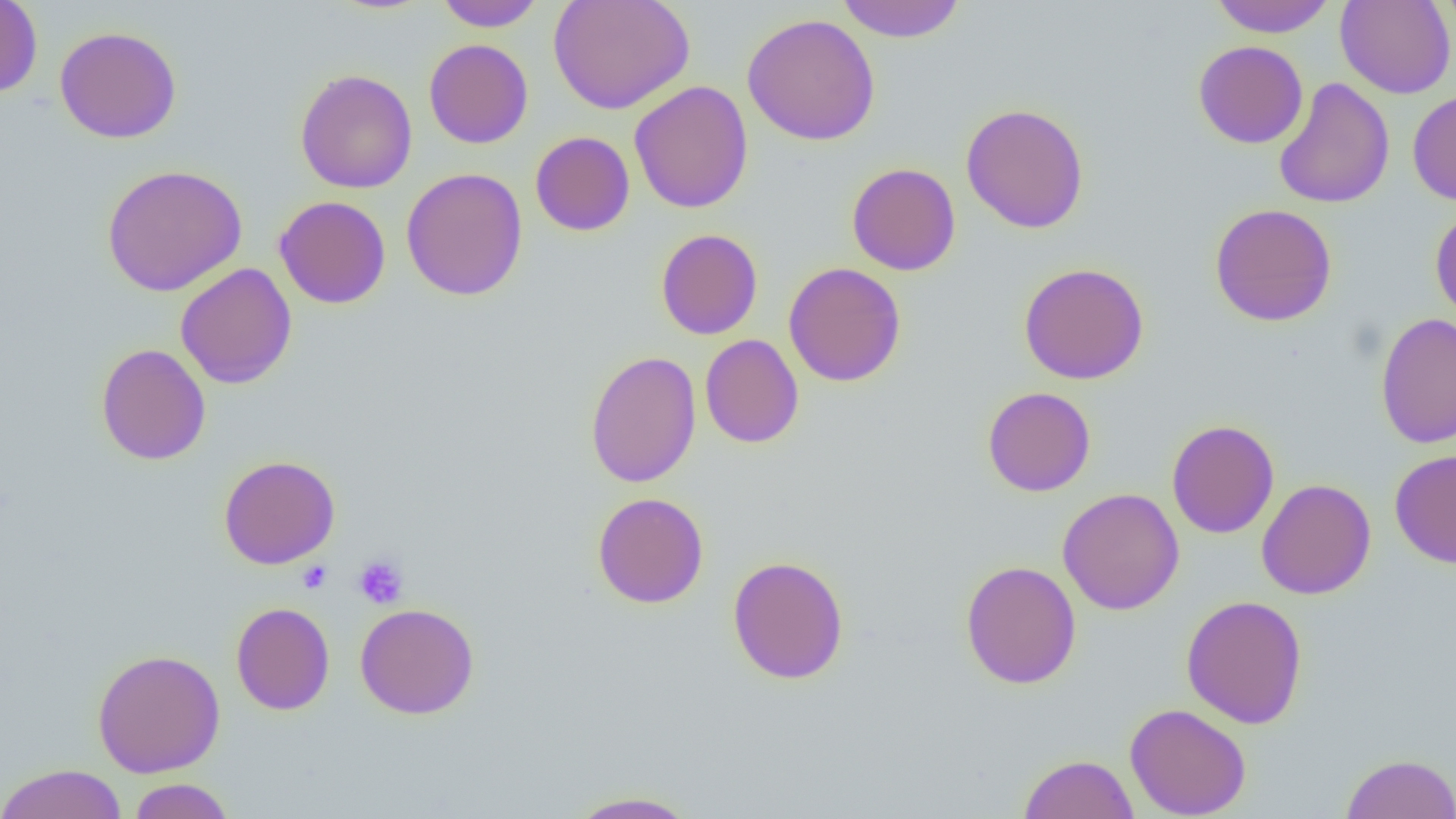

Approximate bounding boxes as (x1,y1)-(x2,y2) corner pairs in pixels. Platelet locations: (352,553)-(409,610), (297,560)-(332,593). Uninfected red blood cell locations: (0,0)-(43,99), (434,0)-(546,32), (549,0)-(695,114), (835,0)-(967,43), (1209,0)-(1337,37), (1335,0)-(1456,99), (1435,0)-(1456,40), (742,13)-(880,146), (54,26)-(182,143), (424,38)-(533,149), (1193,40)-(1308,149), (295,68)-(418,193), (1273,77)-(1395,209), (629,81)-(754,214), (1407,89)-(1456,206), (960,102)-(1090,234), (530,131)-(635,236), (847,162)-(961,276), (102,164)-(248,297), (401,167)-(528,301), (274,195)-(391,309), (1210,203)-(1338,326), (1430,205)-(1456,324), (655,228)-(763,340), (783,262)-(906,387), (1019,262)-(1150,385), (175,263)-(297,389), (1375,312)-(1456,449), (700,334)-(804,449), (96,343)-(211,465), (585,350)-(702,488), (982,386)-(1096,497), (1166,419)-(1279,539), (1389,448)-(1456,568), (218,455)-(341,569), (1256,478)-(1376,600), (1058,487)-(1184,614), (593,492)-(709,609), (727,555)-(849,685), (960,560)-(1082,689), (1181,595)-(1308,729), (231,602)-(335,716), (355,603)-(479,719), (92,648)-(226,778), (1124,703)-(1252,819), (1018,753)-(1139,819), (1342,753)-(1456,819), (0,763)-(128,819), (127,778)-(236,819), (564,790)-(702,818). Slide-level diagnosis: no evidence of blood parasites. Single field of view. Image is 1456×819 pixels. 1000x magnification. Optical microscopy. Thin blood film.